Look for parasitized red blood cells.
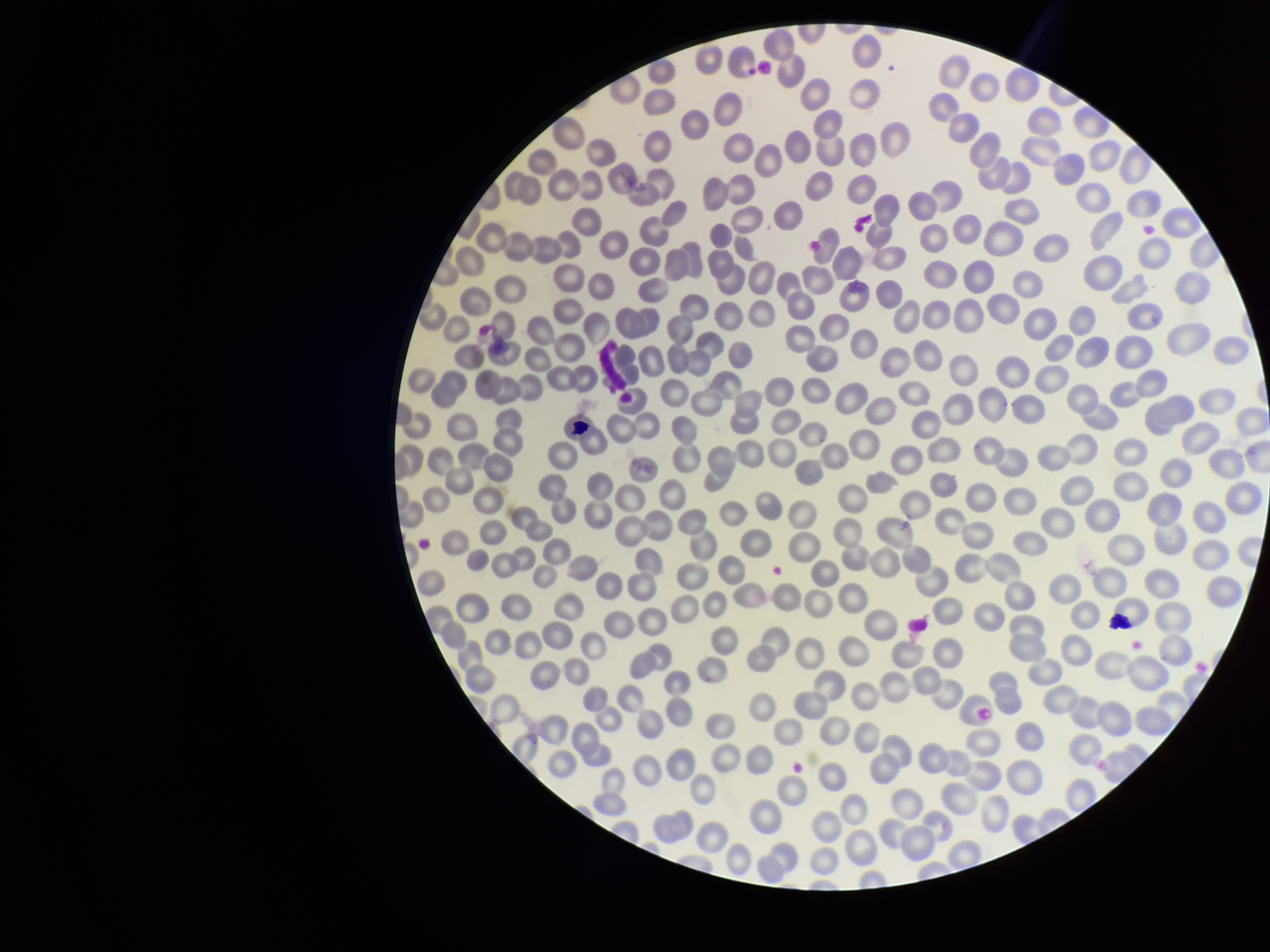

None detected.

Patient malaria status: negative. Parasitized red blood cell count: 0. Smartphone photograph taken through the eyepiece of a microscope. Single field of view. Giemsa stain. Preparation: thin smear. Image is 1270×952 pixels. Red blood cell count: 296.